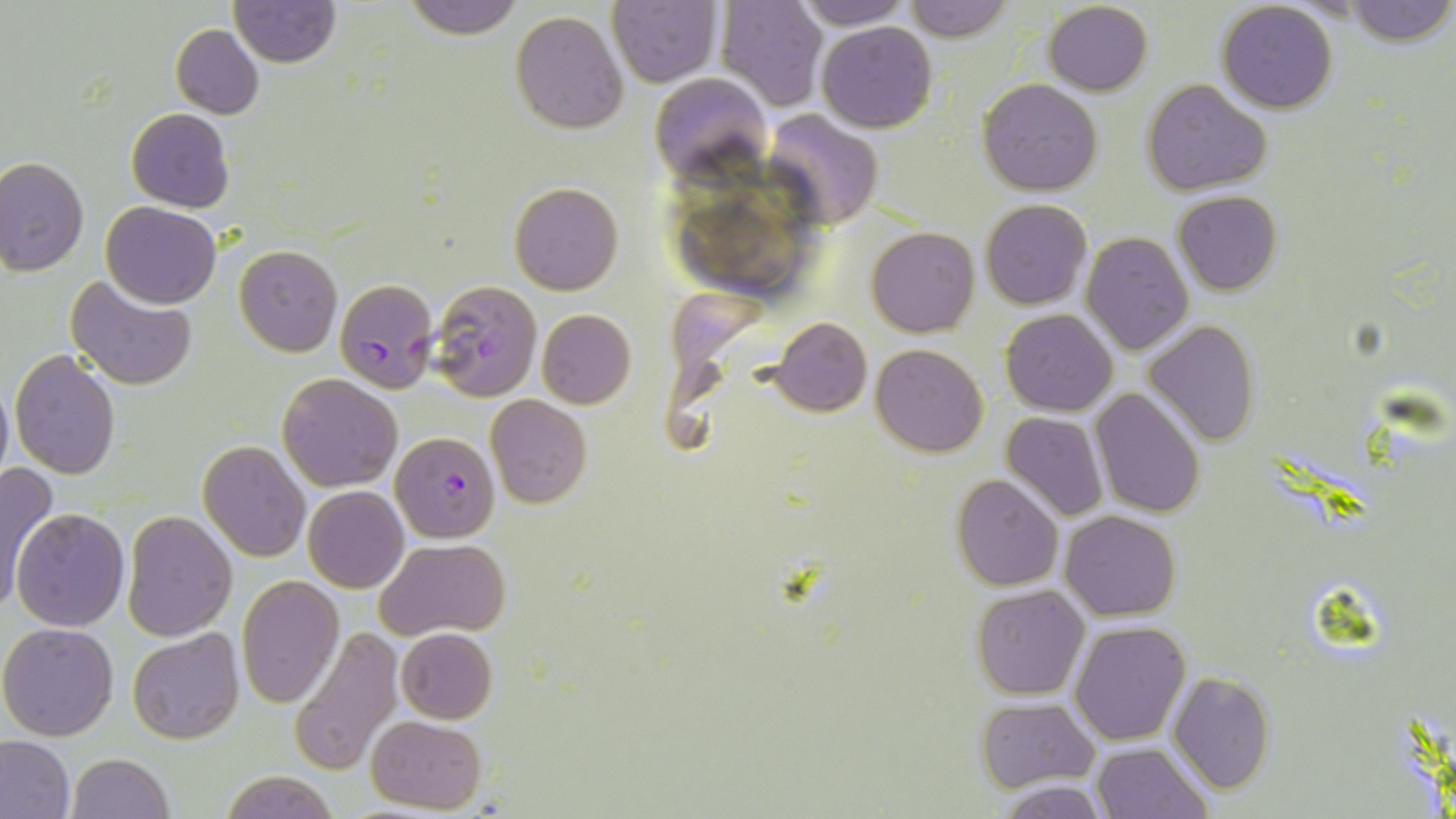

Approximate bounding boxes as (x1,y1)-(x2,y2) corner pairs in pixels. Uninfected red blood cell locations: (230,0)-(340,67), (401,0)-(525,37), (607,0)-(723,88), (788,0)-(911,30), (900,0)-(1014,42), (1341,0)-(1454,45), (715,1)-(827,111), (1044,2)-(1152,96), (1215,2)-(1338,114), (510,9)-(629,134), (817,22)-(937,133), (171,24)-(263,119), (648,74)-(771,185), (977,78)-(1103,196), (1143,79)-(1273,198), (126,108)-(235,213), (763,111)-(884,230), (0,157)-(89,275), (508,181)-(625,296), (1173,190)-(1282,295), (979,199)-(1093,310), (102,202)-(220,309), (866,226)-(980,337), (1081,232)-(1193,356), (233,245)-(343,357), (64,274)-(197,391), (536,309)-(636,409), (1001,309)-(1117,416), (773,317)-(871,417), (1143,319)-(1259,447), (870,344)-(990,457), (10,349)-(121,479), (0,372)-(13,492), (277,373)-(403,492), (1090,388)-(1207,518), (485,395)-(593,509), (1002,411)-(1109,522), (198,440)-(312,563), (0,463)-(61,616), (951,474)-(1064,590), (302,486)-(409,593), (12,507)-(131,631), (121,511)-(238,641), (1060,511)-(1181,620), (375,538)-(511,641), (236,576)-(345,709), (971,585)-(1090,699), (1068,620)-(1191,746), (0,622)-(120,741), (291,625)-(404,775), (394,627)-(498,724), (128,628)-(243,746), (1168,672)-(1277,794), (977,698)-(1098,793), (365,715)-(486,813), (0,734)-(74,819), (1090,742)-(1214,819), (66,753)-(176,818), (216,768)-(340,819), (995,778)-(1114,817). Plasmodium falciparum-infected red blood cell locations: (335,278)-(438,392), (427,279)-(542,402), (392,429)-(499,542). Slide-level diagnosis: Plasmodium falciparum. May-Grünwald-Giemsa stain. Optical microscopy. Image is 1456×819 pixels. Captured at 1000x magnification. Thin blood film. One field of a larger specimen.